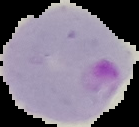

Segmented cell region on a black background. From a thin blood film. Malaria status: parasitized. Image is 139×127 pixels.